Assess this cell for malaria.
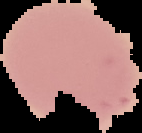

It is parasitized.

image size = 142×133 pixels
image type = segmented cell region on a black background
preparation = thin blood smear